Locate every Plasmodium parasite.
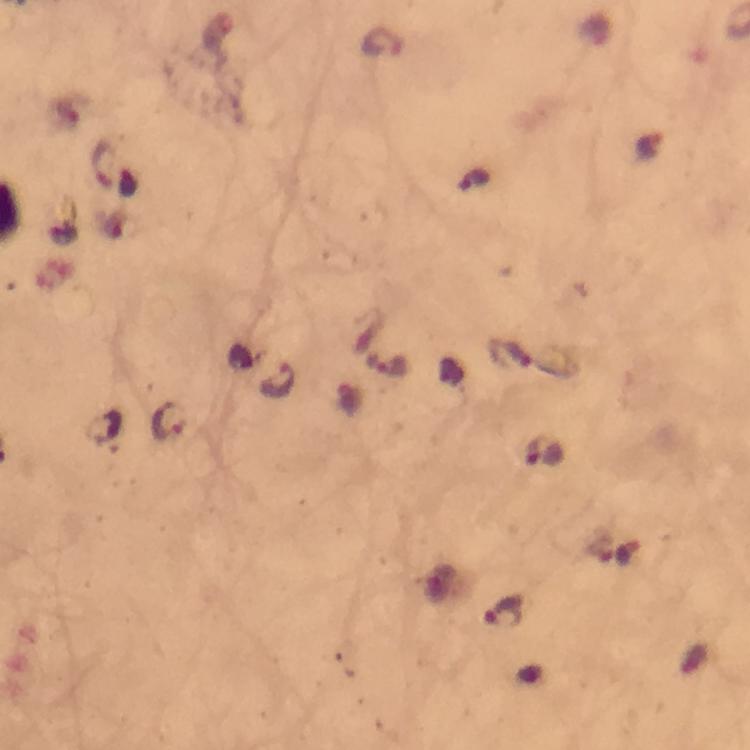

Approximate centers as [x, y] in pixels.
Plasmodium parasites: [382, 41], [649, 147], [104, 162], [474, 180], [509, 353], [386, 365], [279, 379], [169, 420], [544, 451], [503, 611].

Summary:
  - Preparation: thick smear
  - Capture: smartphone photograph through a microscope
  - Cropped from: a single field of view
  - Image size: 750×750 pixels
  - Context: from a malaria diagnostic workup
  - Stain: Giemsa
  - Immersion oil: applied
  - Magnification: 100x